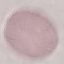

{
  "result": "no malaria parasites seen",
  "image_type": "cell patch, automatically extracted from a larger field of view and resized to 64 × 64 pixels",
  "preparation": "thin blood smear",
  "stain": "Giemsa",
  "capture": "smartphone camera at the microscope eyepiece"
}